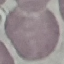
malaria_status: uninfected
preparation: thin smear
capture: smartphone through the microscope eyepiece
image_type: cell patch, automatically extracted from a larger field of view and resized to 64 × 64 pixels
stain: Giemsa